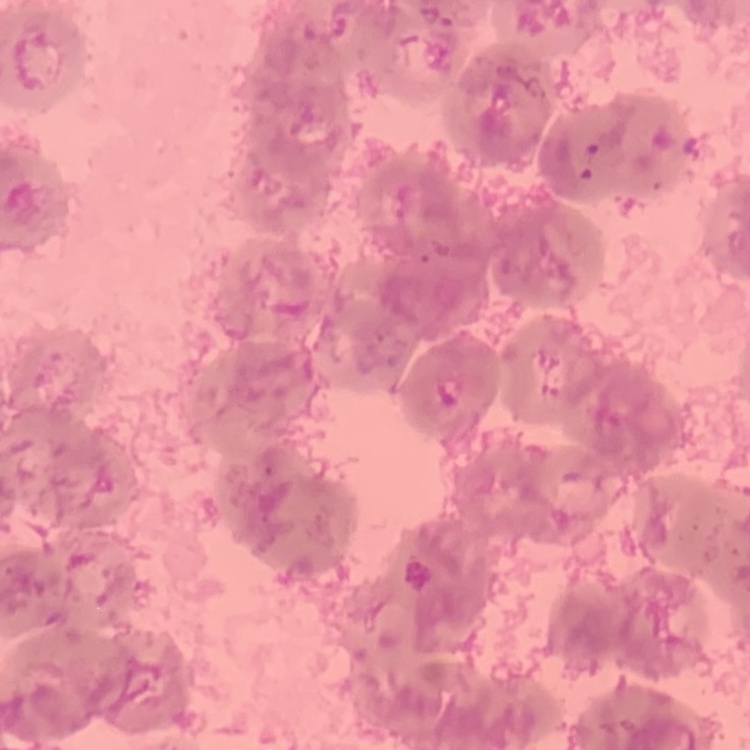

Summary:
  - Erythrocyte morphology: rouleaux formation
  - Image type: one tile cut from a larger photomicrograph
  - Stain: Field's or Giemsa
  - Preparation: thin blood smear